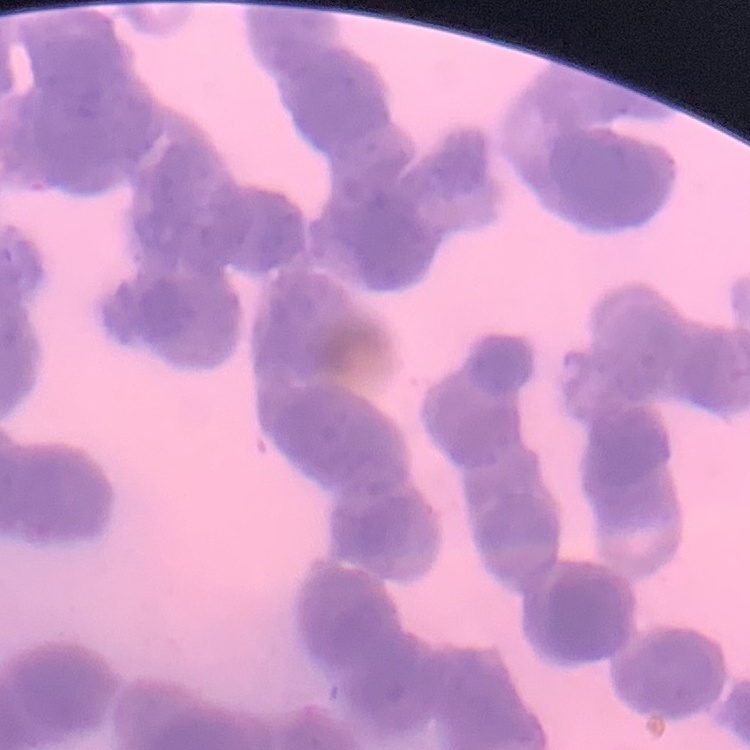 The red blood cells show rouleaux formation. Stained with either Field's or Giemsa. Thin blood film. One tile cut from a larger photomicrograph.